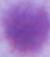

Summary:
  - Magnification: 1000x
  - Identification: red blood cell
  - Modality: photomicrograph